Name the blood parasite species.
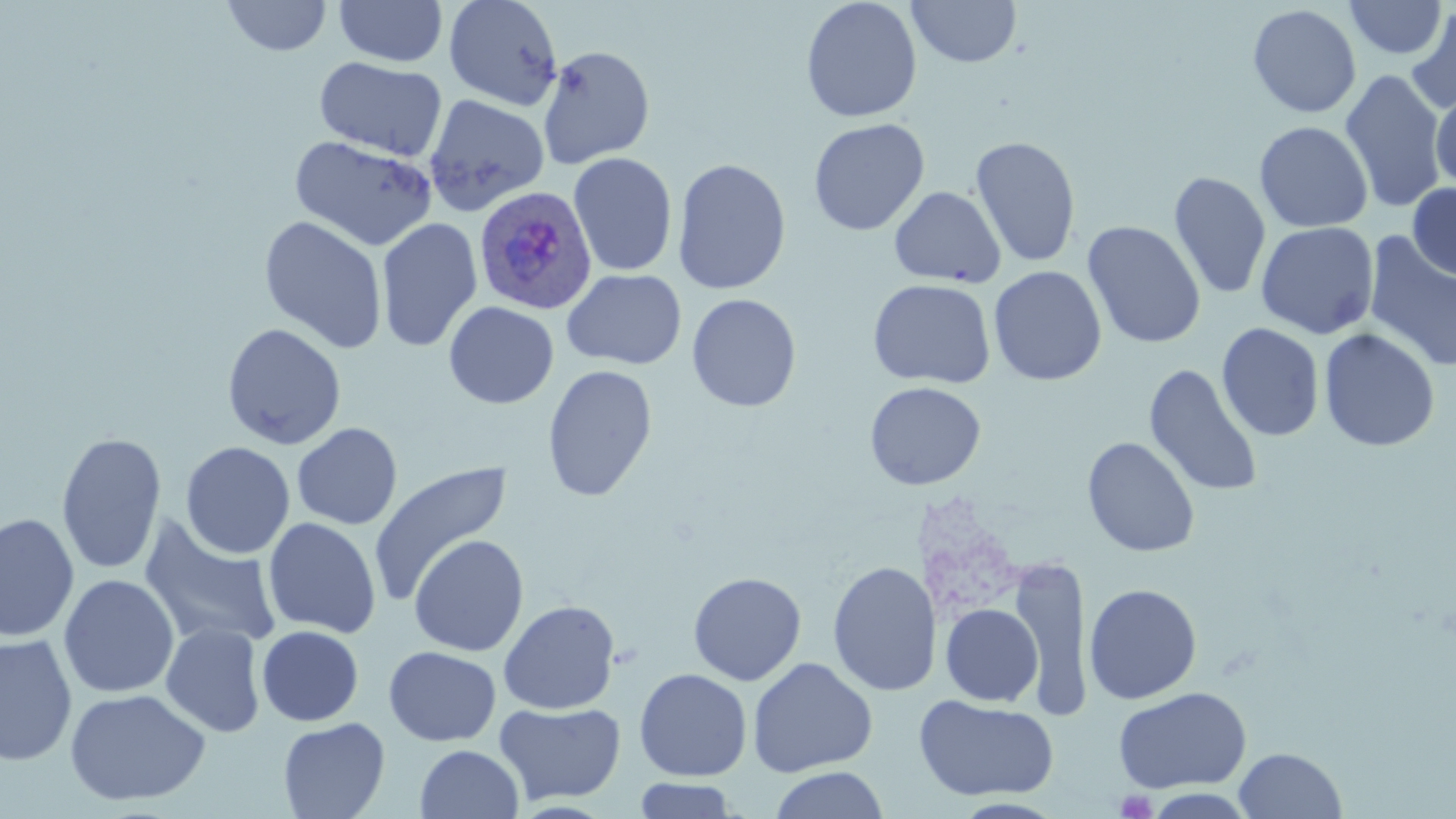

Plasmodium ovale.

Approximate bounding boxes as named x1/y1/x2/y2 corners in pixels. Plasmodium ovale-infected red blood cell locations: (x1=472, y1=188, x2=596, y2=317). Uninfected red blood cell locations: (x1=222, y1=0, x2=333, y2=57), (x1=444, y1=0, x2=564, y2=111), (x1=800, y1=0, x2=922, y2=123), (x1=1342, y1=0, x2=1449, y2=60), (x1=333, y1=1, x2=448, y2=67), (x1=906, y1=1, x2=1022, y2=68), (x1=1247, y1=4, x2=1362, y2=118), (x1=1405, y1=5, x2=1456, y2=116), (x1=537, y1=45, x2=654, y2=169), (x1=314, y1=56, x2=448, y2=161), (x1=1339, y1=68, x2=1449, y2=213), (x1=1430, y1=87, x2=1456, y2=193), (x1=423, y1=94, x2=550, y2=216), (x1=808, y1=118, x2=930, y2=235), (x1=1254, y1=121, x2=1373, y2=233), (x1=289, y1=135, x2=438, y2=251), (x1=969, y1=135, x2=1082, y2=269), (x1=568, y1=152, x2=678, y2=276), (x1=672, y1=158, x2=791, y2=295), (x1=1169, y1=170, x2=1271, y2=301), (x1=1407, y1=183, x2=1456, y2=282), (x1=889, y1=186, x2=1006, y2=287), (x1=258, y1=215, x2=388, y2=354), (x1=376, y1=217, x2=482, y2=352), (x1=1083, y1=221, x2=1205, y2=349), (x1=1255, y1=221, x2=1379, y2=339), (x1=1363, y1=232, x2=1456, y2=373), (x1=989, y1=265, x2=1107, y2=386), (x1=562, y1=269, x2=687, y2=370), (x1=867, y1=278, x2=996, y2=388), (x1=686, y1=293, x2=802, y2=413), (x1=444, y1=301, x2=558, y2=409), (x1=222, y1=323, x2=347, y2=450), (x1=1217, y1=323, x2=1325, y2=442), (x1=1319, y1=328, x2=1440, y2=451), (x1=541, y1=364, x2=658, y2=502), (x1=1144, y1=364, x2=1263, y2=498), (x1=864, y1=381, x2=986, y2=490), (x1=292, y1=423, x2=402, y2=530), (x1=56, y1=431, x2=167, y2=575), (x1=1081, y1=436, x2=1200, y2=557), (x1=180, y1=441, x2=295, y2=559), (x1=370, y1=460, x2=513, y2=607), (x1=0, y1=512, x2=79, y2=643), (x1=139, y1=516, x2=283, y2=652), (x1=263, y1=517, x2=382, y2=639), (x1=409, y1=534, x2=529, y2=657), (x1=1008, y1=556, x2=1091, y2=716), (x1=827, y1=560, x2=941, y2=697), (x1=688, y1=572, x2=807, y2=685), (x1=59, y1=574, x2=179, y2=699), (x1=1083, y1=583, x2=1202, y2=704), (x1=498, y1=600, x2=620, y2=714), (x1=941, y1=603, x2=1043, y2=707), (x1=160, y1=622, x2=266, y2=738), (x1=257, y1=625, x2=364, y2=726), (x1=0, y1=633, x2=77, y2=766), (x1=384, y1=646, x2=501, y2=747), (x1=747, y1=657, x2=878, y2=778), (x1=633, y1=668, x2=752, y2=781), (x1=64, y1=687, x2=211, y2=807), (x1=1113, y1=687, x2=1252, y2=793), (x1=914, y1=695, x2=1059, y2=801), (x1=493, y1=701, x2=626, y2=806), (x1=277, y1=717, x2=390, y2=819), (x1=416, y1=744, x2=524, y2=819), (x1=1234, y1=747, x2=1347, y2=818), (x1=768, y1=766, x2=890, y2=819), (x1=632, y1=778, x2=741, y2=818). Platelet locations: (x1=1115, y1=789, x2=1158, y2=818). Captured at 1000x magnification. Image is 1456×819 pixels. Thin blood film. Light microscopy. May-Grünwald-Giemsa stain. One field of a larger specimen.